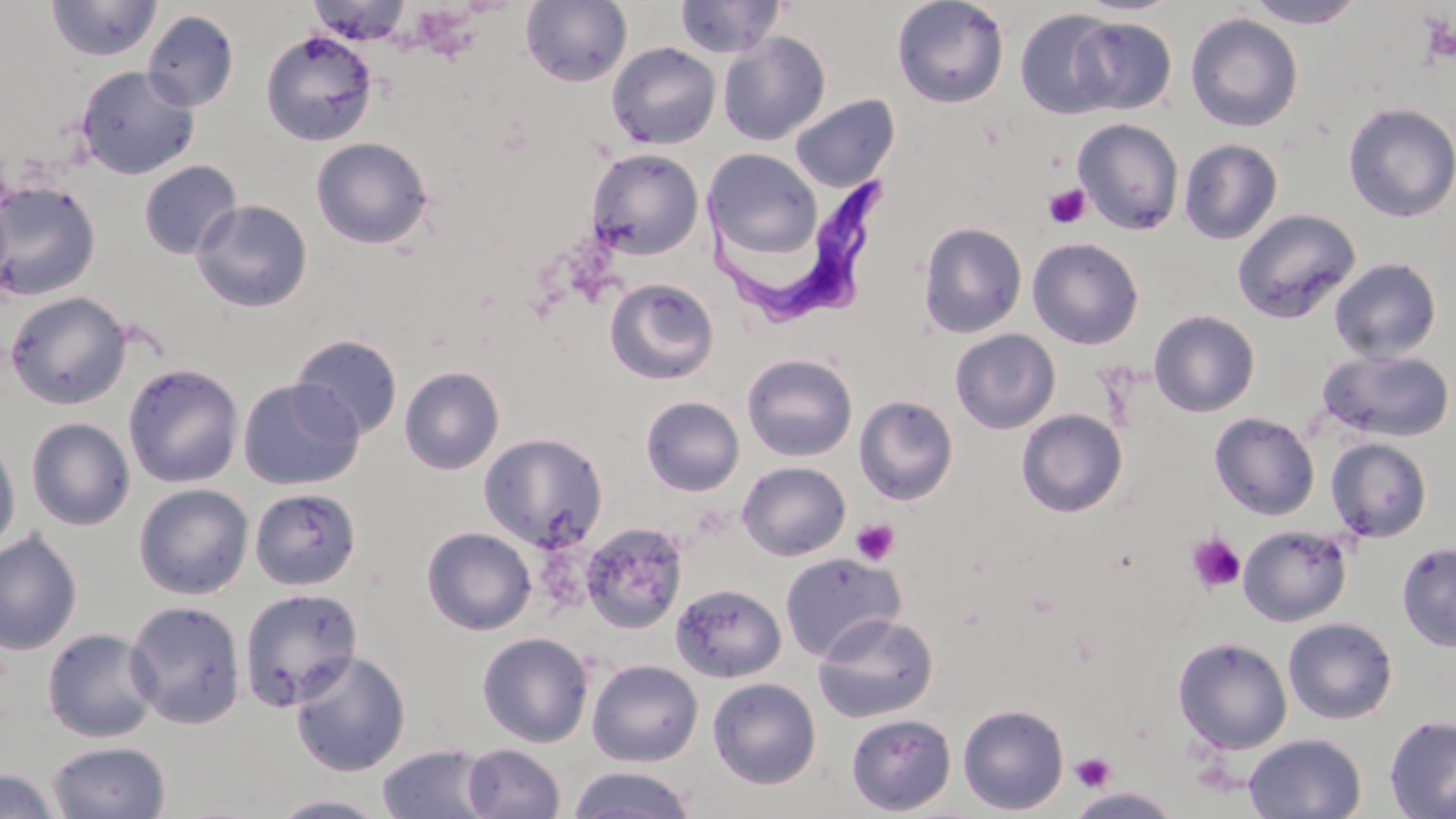

Summary:
  - Coordinate format: approximate bounding boxes as (x1, y1, x2, y2) in pixels
  - Platelet locations: (1048, 150, 1069, 171), (1043, 183, 1091, 229), (850, 518, 900, 566), (1186, 534, 1246, 594), (1070, 752, 1116, 793)
  - Uninfected red blood cell locations: (674, 0, 786, 59), (891, 0, 1010, 108), (46, 1, 162, 63), (307, 1, 414, 46), (520, 1, 632, 85), (1244, 1, 1366, 28), (142, 9, 239, 112), (1014, 9, 1120, 119), (1185, 13, 1303, 132), (1071, 17, 1177, 115), (260, 30, 378, 146), (718, 32, 830, 145), (606, 42, 721, 150), (75, 65, 200, 179), (789, 93, 899, 193), (1343, 102, 1456, 223), (1073, 118, 1184, 235), (311, 136, 433, 249), (1179, 139, 1283, 244), (587, 148, 704, 260), (705, 148, 823, 259), (138, 160, 242, 260), (0, 180, 101, 301), (192, 199, 313, 312), (1232, 209, 1362, 323), (918, 222, 1027, 339), (1027, 237, 1144, 349), (1329, 257, 1442, 363), (605, 277, 719, 385), (5, 291, 132, 409), (1149, 310, 1261, 417), (950, 328, 1060, 434), (290, 334, 404, 441), (1317, 348, 1455, 443), (741, 353, 858, 462), (122, 362, 244, 488), (399, 365, 504, 475), (237, 377, 364, 490), (854, 395, 958, 505), (641, 396, 744, 496), (1016, 409, 1128, 517), (1209, 412, 1320, 520), (25, 417, 136, 530), (479, 433, 608, 551), (0, 434, 21, 556), (1326, 437, 1432, 543), (738, 461, 851, 561), (133, 483, 253, 599), (249, 487, 361, 591), (579, 522, 689, 634), (1237, 524, 1352, 627), (422, 526, 537, 635), (0, 530, 82, 656), (1396, 542, 1456, 652), (779, 551, 905, 662), (670, 582, 787, 683), (238, 587, 363, 710), (124, 600, 247, 729), (813, 612, 938, 723), (1282, 617, 1398, 724), (42, 626, 160, 743), (477, 632, 594, 747), (1172, 636, 1293, 754), (289, 651, 411, 777), (587, 659, 703, 766), (708, 677, 821, 789), (958, 703, 1069, 815), (846, 713, 956, 815), (1384, 714, 1456, 819), (1243, 733, 1366, 818), (47, 740, 171, 819), (461, 743, 565, 819), (377, 744, 497, 819), (566, 767, 698, 819), (0, 768, 61, 819), (1066, 787, 1182, 818), (269, 793, 394, 819)
  - Trypanosoma brucei locations: (692, 174, 893, 332)
  - Slide-level diagnosis: Trypanosoma brucei
  - Preparation: thin blood film
  - Field of view: one of a larger specimen
  - Magnification: 1000x
  - Modality: optical microscopy
  - Stain: May-Grünwald-Giemsa
  - Image size: 1456×819 pixels